Identify the blood parasite species.
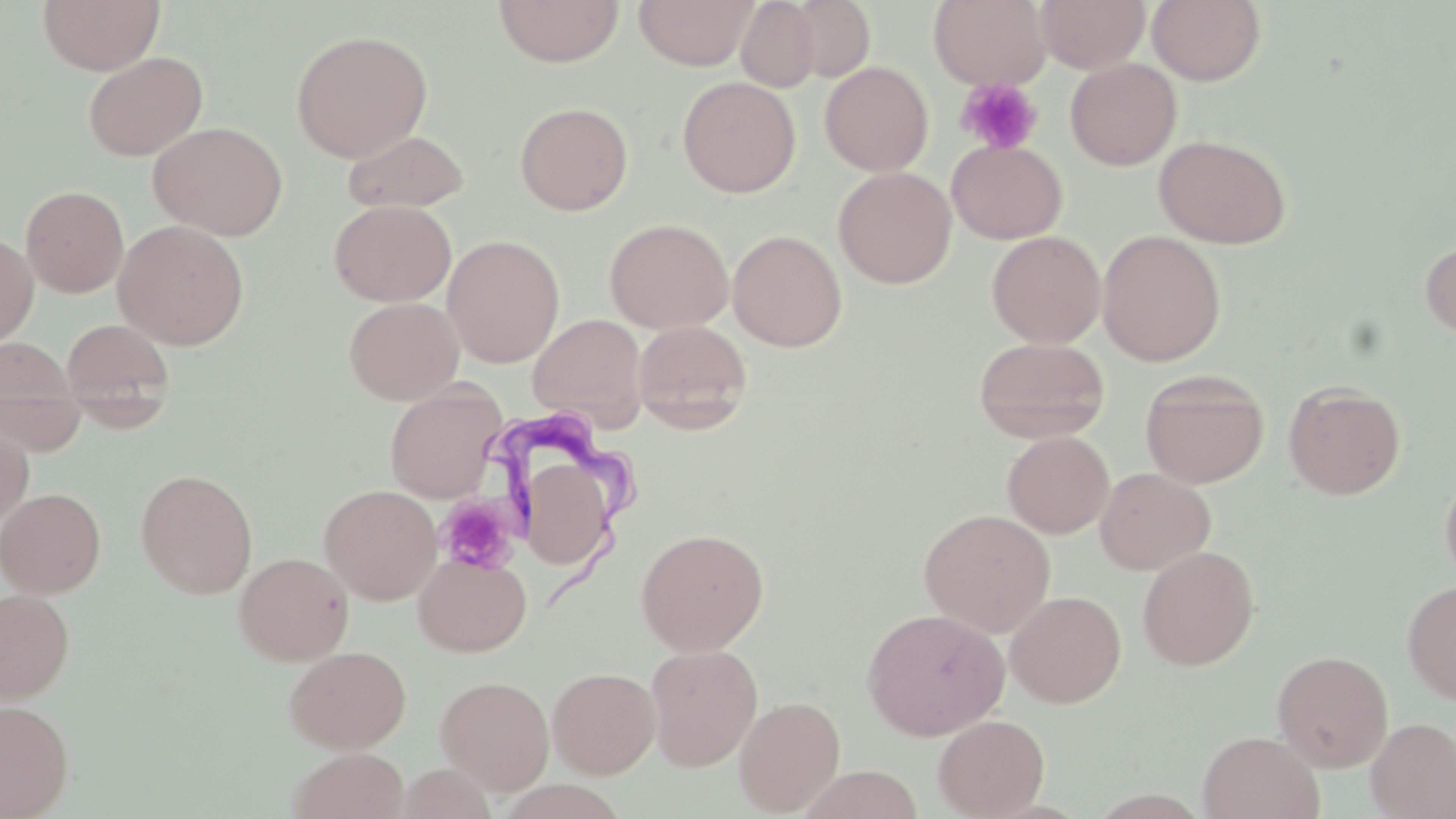
Trypanosoma brucei.

Approximate bounding boxes as (x1, y1, x2, y2) in pixels. Uninfected red blood cell locations: (37, 0, 164, 75), (493, 0, 624, 67), (633, 0, 760, 70), (736, 0, 821, 93), (785, 0, 876, 85), (928, 0, 1051, 90), (1036, 0, 1150, 72), (1147, 0, 1267, 86), (291, 29, 432, 162), (83, 51, 207, 161), (1065, 58, 1182, 170), (820, 61, 933, 176), (677, 76, 800, 197), (515, 101, 633, 215), (148, 121, 288, 240), (342, 129, 469, 213), (1154, 134, 1291, 249), (947, 139, 1067, 244), (833, 166, 956, 288), (21, 185, 129, 297), (329, 200, 457, 306), (604, 218, 733, 334), (113, 219, 250, 350), (727, 229, 847, 351), (1096, 230, 1227, 365), (987, 231, 1106, 347), (0, 232, 38, 350), (443, 235, 564, 367), (1420, 238, 1456, 342), (344, 296, 464, 405), (528, 313, 647, 429), (60, 317, 176, 423), (634, 320, 752, 431), (973, 336, 1109, 443), (0, 338, 86, 453), (1140, 370, 1269, 489), (1283, 380, 1406, 499), (385, 383, 505, 503), (0, 422, 34, 531), (1003, 431, 1114, 538), (524, 460, 613, 561), (1439, 466, 1456, 591), (1095, 467, 1216, 575), (136, 469, 258, 598), (319, 484, 441, 604), (0, 487, 106, 597), (918, 508, 1056, 637), (635, 527, 770, 656), (1137, 545, 1260, 670), (234, 551, 354, 665), (414, 553, 532, 656), (1401, 581, 1456, 704), (0, 588, 75, 702), (1005, 590, 1127, 708), (862, 607, 1009, 741), (645, 644, 763, 771), (284, 645, 411, 753), (1272, 650, 1393, 772), (547, 667, 661, 778), (436, 675, 555, 794), (733, 695, 846, 815), (0, 699, 74, 818), (933, 714, 1049, 818), (1366, 717, 1456, 818), (1197, 730, 1324, 819), (287, 748, 409, 819), (395, 762, 498, 819), (797, 765, 924, 819). Platelet locations: (955, 77, 1043, 155), (436, 494, 519, 574). Trypanosoma brucei locations: (487, 408, 642, 608). May-Grünwald-Giemsa-stained preparation. Captured at 1000x magnification. Thin blood film. Light microscopy. One field of a larger specimen. Image is 1456×819 pixels.